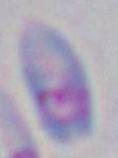

Summary:
  - Magnification: 1000x
  - Modality: photomicrograph
  - Identification: Toxoplasma gondii